Report the malaria status of this cell.
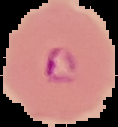

It is parasitized.

preparation = thin blood smear
image size = 118×127 pixels
image type = segmented cell region on a black background